Classify this cell by malaria status.
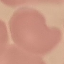
Uninfected.

Thin smear of blood. Automatically extracted cell patch, resized to 64 × 64 pixels. Giemsa stain. Acquired by smartphone through the microscope eyepiece.